State which parasite is depicted.
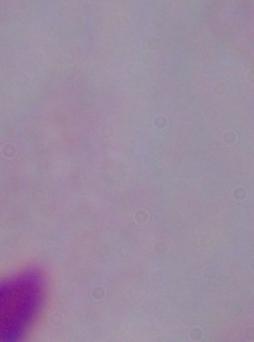

A trichomonad.

magnification: 1000x
modality: photomicrograph